Report the malaria status of this cell.
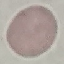

Uninfected.

Summary:
  - Preparation: thin blood smear
  - Stain: Giemsa
  - Image type: cell patch, automatically extracted from a larger field of view and resized to 64 × 64 pixels
  - Capture: smartphone through the microscope eyepiece